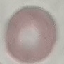

Malaria status: uninfected. Cell patch, automatically extracted from a larger field of view and resized to 64 × 64 pixels. Acquired by smartphone through the microscope eyepiece. Thin smear of blood. Giemsa-stained preparation.